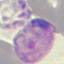 Malaria status: parasitized. Cell patch, automatically extracted from a larger field of view and resized to 64 × 64 pixels. Photographed with a smartphone camera at the microscope eyepiece. Giemsa-stained preparation. Thin blood film.